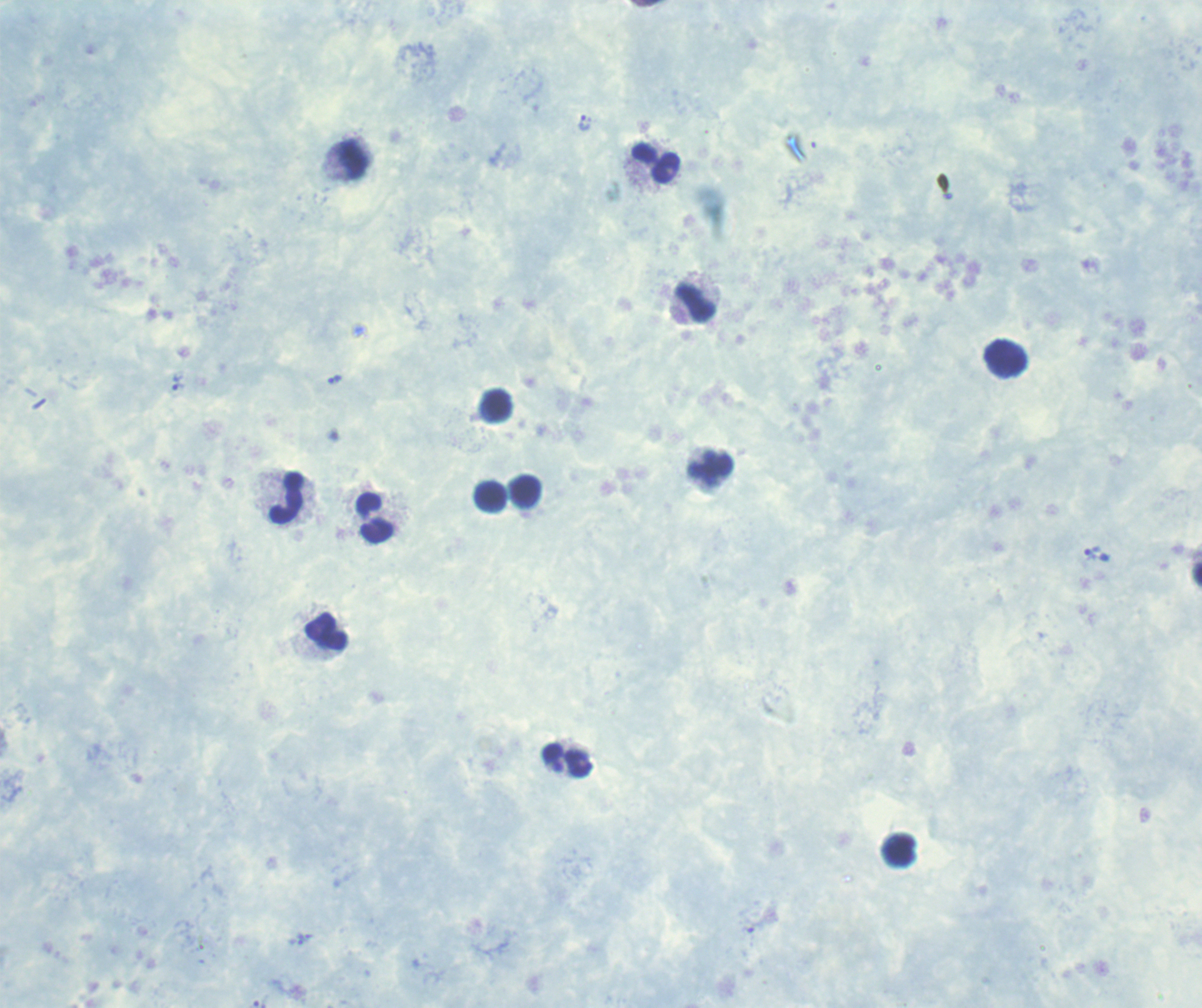
Approximate centers as (x, y) in pixels. Trophozoite locations: (584, 123), (335, 380), (177, 382), (1091, 552). Leukocyte locations: (356, 160), (655, 164), (696, 303), (1006, 359), (497, 406), (711, 468), (526, 491), (491, 497), (287, 499), (376, 519), (326, 632), (567, 760), (899, 849). Thick smear of blood. Previously used in an actual diagnosis. Result: Plasmodium parasites detected. Captured at 100x magnification. Background quality: poor. Romanowsky-stained preparation. Image is 1202×1008 pixels. One field from this slide.